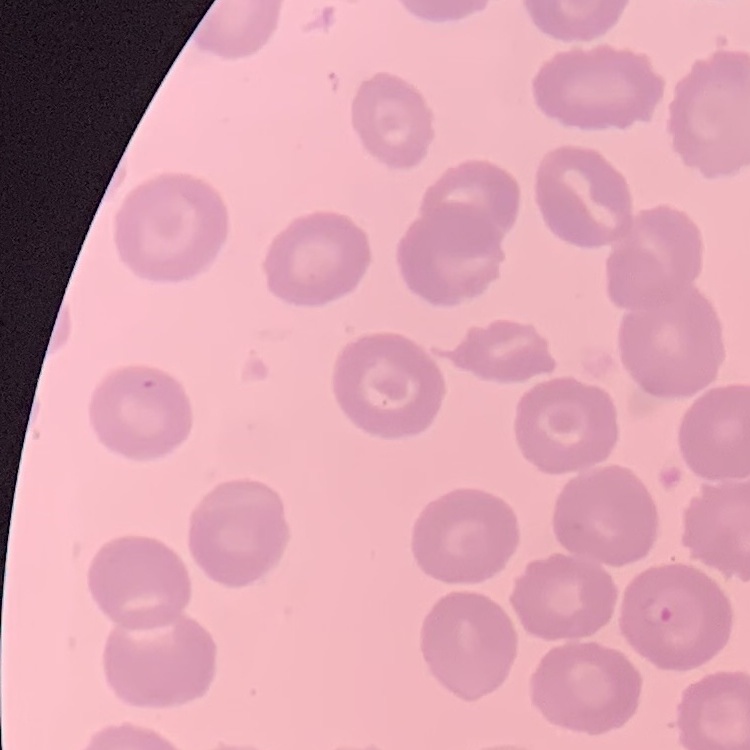
red blood cell morphology = no rouleaux formation
image type = one tile cut from a larger photomicrograph
preparation = thin blood smear
stain = Field's or Giemsa